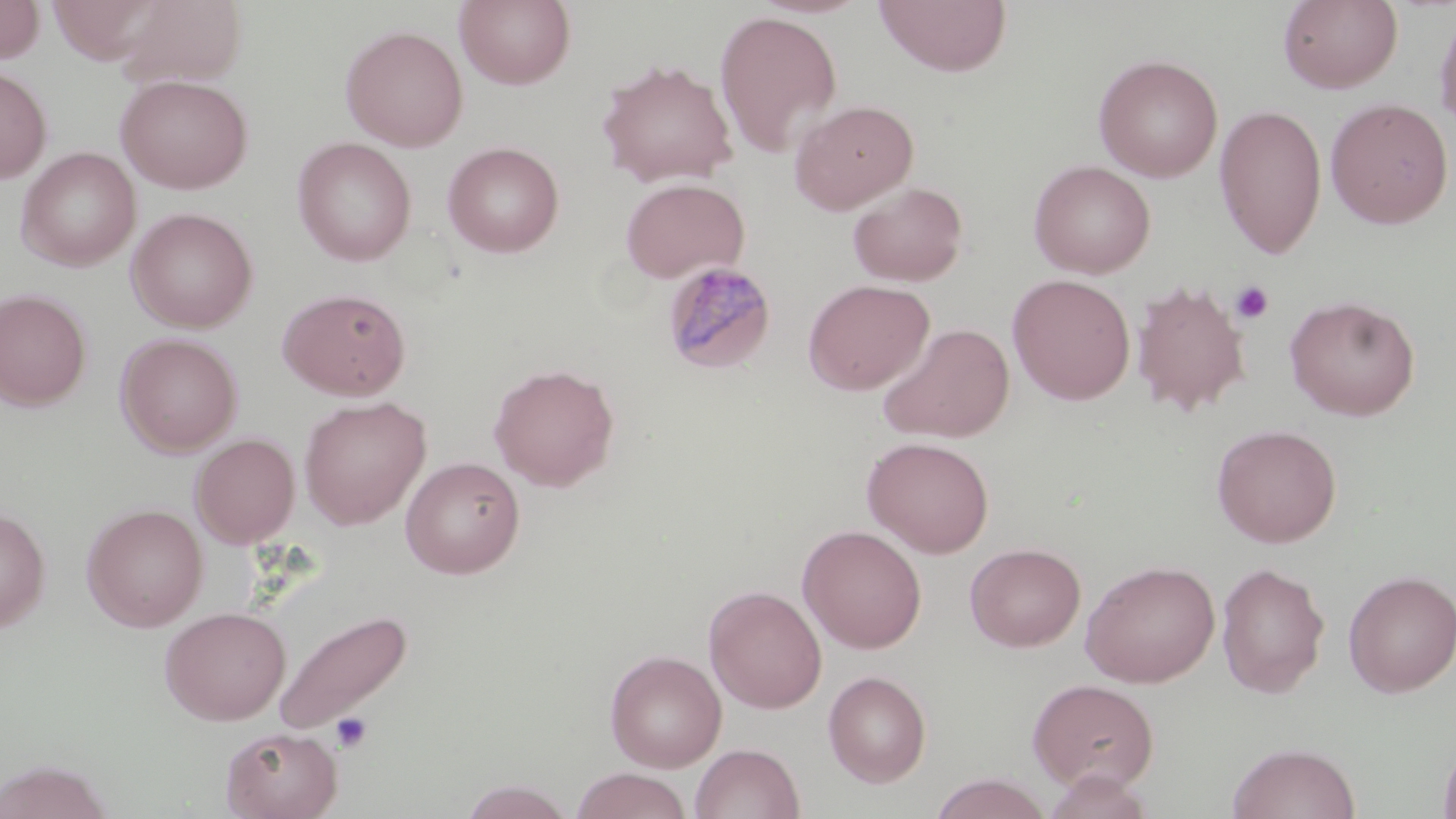
Summary:
  - Coordinate format: approximate bounding boxes as (x1,y1)-(x2,y2) corner pairs in pixels
  - Plasmodium malariae-infected red blood cell locations: (661,261)-(777,375)
  - Platelet locations: (1230,280)-(1274,324), (331,711)-(373,752)
  - Uninfected red blood cell locations: (0,0)-(45,64), (455,0)-(576,89), (874,0)-(1012,77), (1278,0)-(1403,93), (1434,5)-(1456,136), (713,10)-(843,159), (339,24)-(468,152), (1093,53)-(1223,182), (597,59)-(738,188), (0,64)-(52,184), (115,73)-(253,194), (1324,97)-(1454,228), (789,99)-(918,214), (1214,104)-(1327,260), (293,137)-(416,266), (442,141)-(565,258), (16,147)-(141,271), (1029,159)-(1156,279), (619,177)-(750,283), (847,181)-(969,287), (127,207)-(258,333), (1007,274)-(1136,405), (803,279)-(934,395), (1131,280)-(1251,417), (278,287)-(411,400), (0,288)-(93,411), (1283,294)-(1421,420), (877,322)-(1015,444), (116,333)-(243,456), (489,363)-(620,491), (298,396)-(431,529), (1211,423)-(1342,547), (191,433)-(299,548), (862,436)-(995,558), (400,456)-(525,579), (82,503)-(208,632), (0,505)-(51,633), (798,524)-(927,654), (965,542)-(1086,652), (1080,559)-(1220,688), (1216,561)-(1329,698), (1343,569)-(1456,698), (703,585)-(827,713), (159,606)-(291,725), (271,607)-(413,738), (605,649)-(727,771), (823,670)-(932,787), (1027,678)-(1159,792), (221,726)-(343,819), (1437,733)-(1456,819), (1227,742)-(1361,819), (690,743)-(805,819), (0,759)-(115,819), (570,768)-(693,819), (1041,769)-(1158,819), (928,773)-(1051,818), (459,779)-(576,818)
  - Slide-level diagnosis: Plasmodium malariae
  - Stain: May-Grünwald-Giemsa
  - Modality: light microscopy
  - Image size: 1456×819 pixels
  - Magnification: 1000x
  - Field of view: single
  - Preparation: thin blood film